Point out each Plasmodium parasite and each leukocyte.
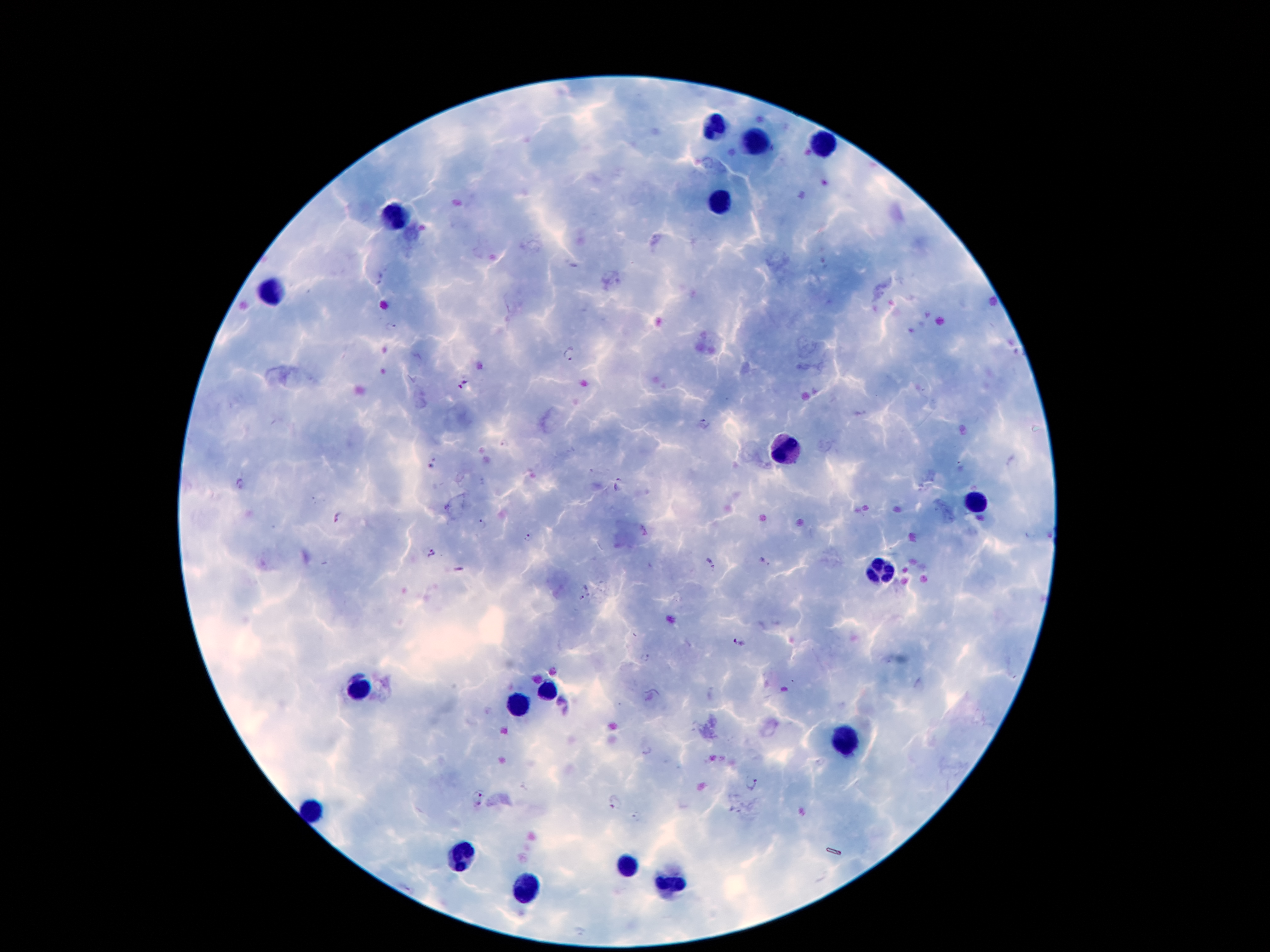
Approximate centers as [x, y] in pixels.
Plasmodium parasites: [379, 278], [391, 324], [571, 353], [464, 384], [702, 424], [432, 463], [618, 484], [336, 517], [481, 524], [529, 538], [431, 552], [709, 562], [581, 599], [740, 641], [646, 658], [751, 784], [478, 797], [614, 803].
Leukocytes: [714, 126], [752, 144], [821, 146], [720, 204], [397, 212], [271, 288], [787, 449], [979, 502], [876, 570], [359, 684], [546, 691], [519, 707], [844, 741], [313, 809], [462, 856], [628, 867], [674, 884], [527, 889].

Summary:
  - Magnification: 100x
  - Field of view: one from this slide
  - Image size: 1270×952 pixels
  - Capture: smartphone camera through the microscope eyepiece
  - Patient malaria status: positive for Plasmodium falciparum
  - Stain: Giemsa
  - Preparation: thick blood smear